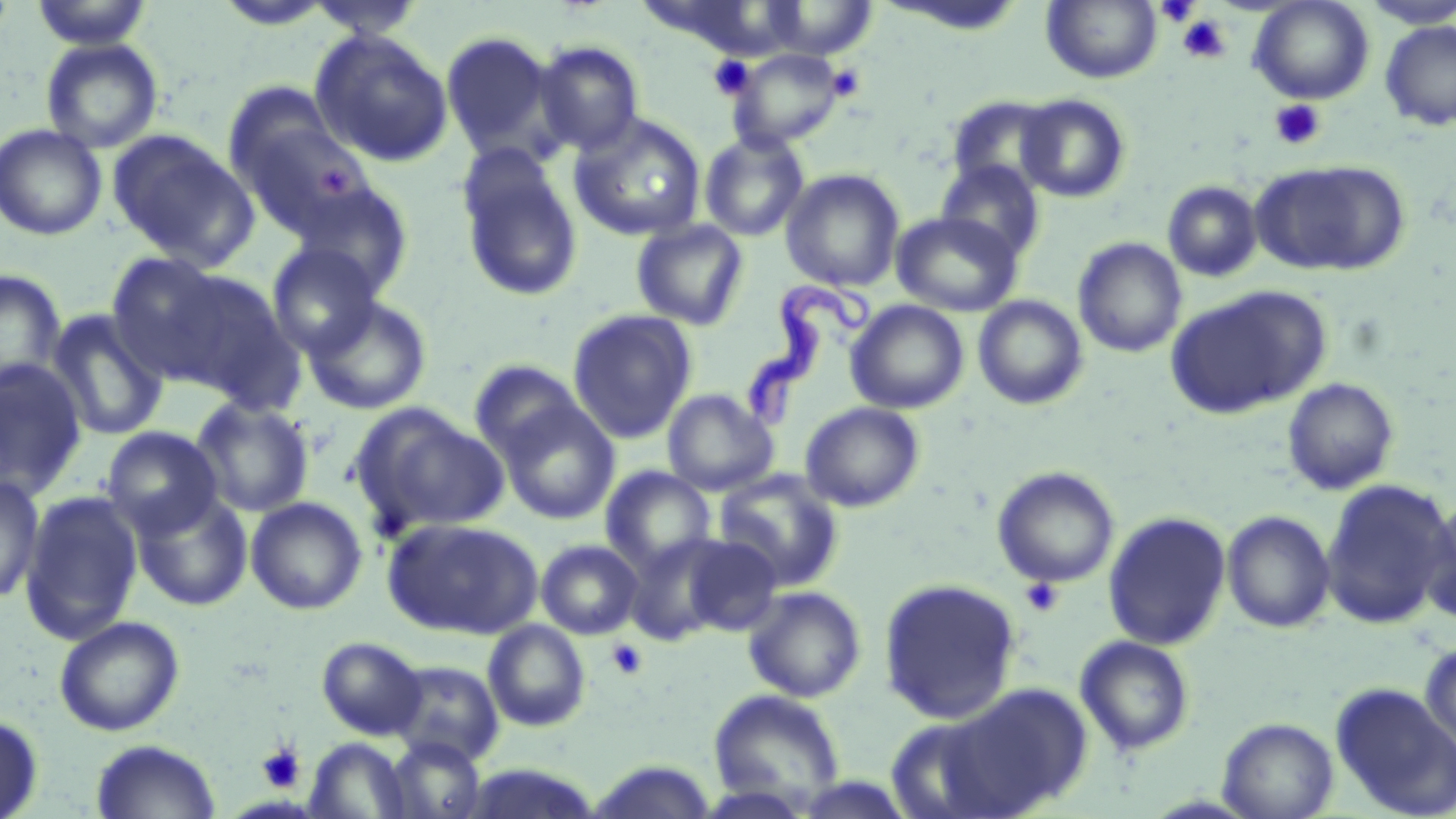
Summary:
  - Coordinate format: approximate bounding boxes as (x1, y1, x2, y2) in pixels
  - Uninfected red blood cell locations: (30, 0, 155, 50), (302, 0, 427, 40), (1041, 0, 1162, 84), (1248, 0, 1375, 105), (762, 1, 879, 59), (1359, 1, 1456, 29), (1379, 20, 1456, 131), (440, 29, 562, 165), (310, 30, 454, 166), (41, 38, 163, 154), (533, 41, 644, 156), (729, 48, 846, 149), (1016, 93, 1131, 203), (946, 94, 1062, 193), (569, 113, 707, 241), (234, 117, 372, 239), (0, 123, 107, 241), (108, 130, 258, 270), (698, 130, 810, 242), (456, 150, 584, 303), (1251, 159, 1408, 277), (935, 160, 1047, 265), (781, 169, 905, 292), (288, 181, 415, 299), (1162, 181, 1263, 282), (892, 211, 1023, 316), (631, 219, 750, 330), (1073, 237, 1187, 358), (266, 245, 383, 360), (105, 252, 238, 383), (0, 268, 67, 399), (151, 268, 304, 409), (1165, 285, 1330, 420), (303, 295, 433, 415), (973, 295, 1088, 410), (846, 300, 969, 414), (45, 309, 168, 442), (567, 309, 698, 444), (0, 357, 88, 503), (469, 360, 588, 465), (1282, 378, 1400, 496), (663, 388, 779, 495), (191, 398, 315, 518), (495, 399, 621, 524), (799, 401, 925, 512), (349, 403, 509, 538), (101, 426, 224, 538), (601, 466, 716, 573), (992, 466, 1119, 588), (713, 470, 845, 592), (0, 475, 45, 605), (1319, 478, 1454, 629), (19, 490, 144, 646), (132, 491, 253, 611), (1418, 492, 1456, 628), (246, 497, 367, 615), (1222, 510, 1336, 633), (1102, 511, 1232, 651), (382, 517, 543, 639), (679, 534, 783, 636), (625, 535, 729, 646), (536, 539, 644, 640), (878, 578, 1022, 723), (743, 585, 867, 702), (54, 616, 185, 736), (483, 620, 591, 732), (1075, 635, 1195, 756), (316, 636, 428, 740), (1419, 637, 1455, 758), (389, 660, 504, 766), (1330, 682, 1456, 819), (943, 683, 1093, 816), (709, 689, 846, 809), (0, 713, 43, 819), (882, 713, 1011, 819), (1217, 717, 1339, 819), (384, 737, 486, 819), (306, 738, 411, 818), (90, 739, 221, 819), (586, 759, 719, 819)
  - Trypanosoma brucei locations: (746, 259, 879, 433)
  - Platelet locations: (1155, 2, 1199, 25), (1176, 16, 1230, 64), (707, 55, 754, 99), (825, 63, 866, 101), (1270, 100, 1326, 150), (317, 162, 357, 197), (1019, 578, 1064, 618), (606, 638, 649, 679), (256, 743, 305, 791)
  - Slide-level diagnosis: Trypanosoma brucei
  - Field of view: one of a larger specimen
  - Preparation: thin blood film
  - Image size: 1456×819 pixels
  - Stain: May-Grünwald-Giemsa
  - Magnification: 1000x
  - Modality: optical microscopy